Give the position of every Plasmodium parasite visible.
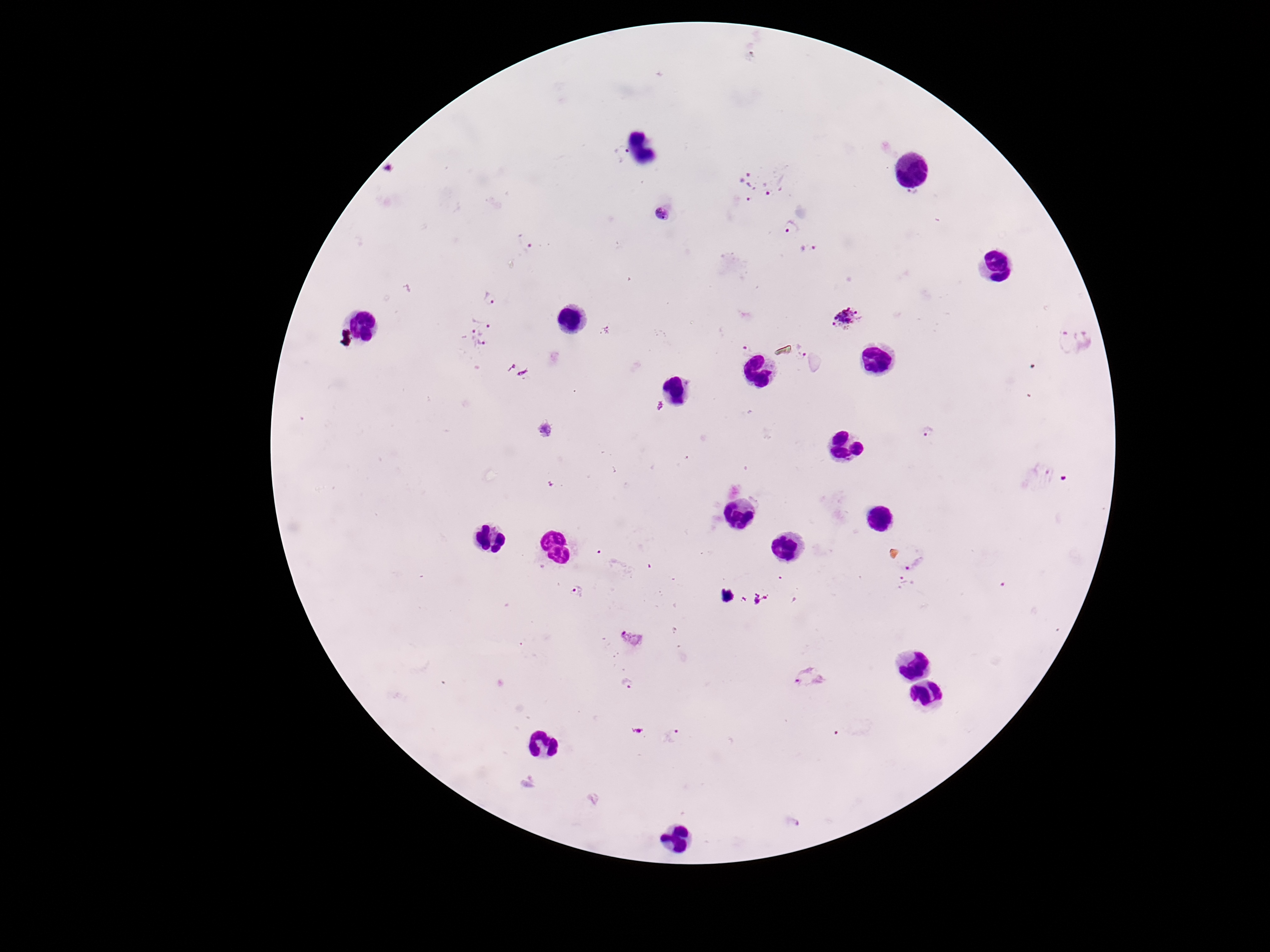
Approximate object centers, in pixels from the top-left corner.
Plasmodium parasites: (x=622, y=154), (x=762, y=184), (x=914, y=194), (x=663, y=213), (x=790, y=227), (x=526, y=244), (x=809, y=249), (x=490, y=299), (x=847, y=318), (x=477, y=332), (x=604, y=332), (x=1073, y=341), (x=747, y=348), (x=800, y=349), (x=517, y=370), (x=660, y=406), (x=545, y=429), (x=927, y=430), (x=914, y=561), (x=904, y=582), (x=578, y=592), (x=633, y=637), (x=809, y=675), (x=628, y=684), (x=675, y=734), (x=794, y=821).

Summary:
  - Patient malaria status: positive
  - Magnification: 100x
  - Stain: Giemsa
  - Capture: smartphone camera through the microscope eyepiece
  - Image size: 1270×952 pixels
  - Field of view: single
  - Preparation: thick blood smear